Locate every blood parasite and identify its species.
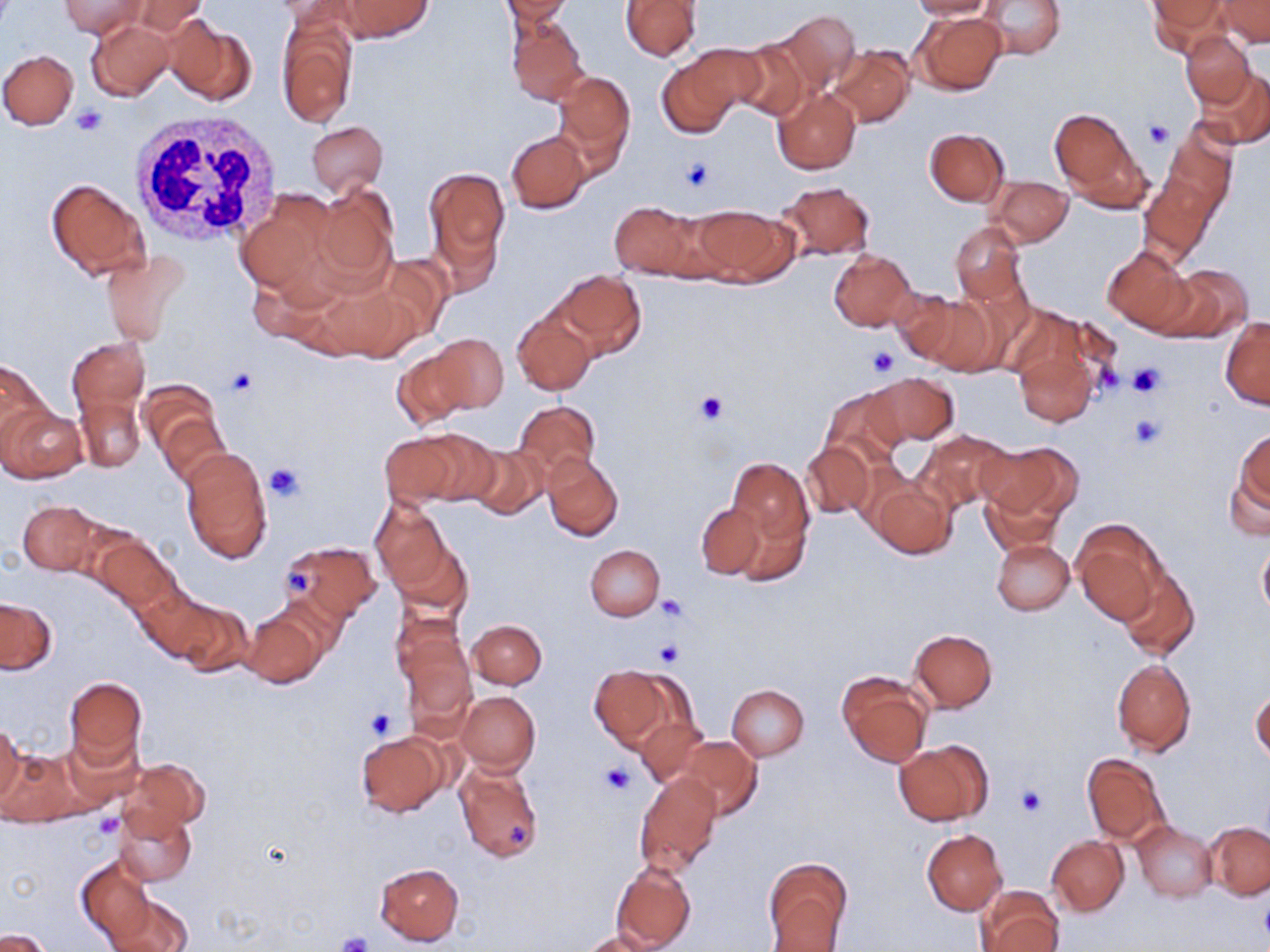

No blood parasites observed.

Approximate bounding boxes as named x1/y1/x2/y2 corners in pixels. Uninfected red blood cell locations: (x1=61, y1=0, x2=143, y2=38), (x1=120, y1=0, x2=213, y2=37), (x1=336, y1=0, x2=432, y2=41), (x1=501, y1=0, x2=573, y2=24), (x1=908, y1=0, x2=1000, y2=20), (x1=980, y1=0, x2=1066, y2=60), (x1=1148, y1=0, x2=1227, y2=53), (x1=621, y1=1, x2=700, y2=60), (x1=1218, y1=1, x2=1270, y2=48), (x1=774, y1=10, x2=860, y2=94), (x1=913, y1=11, x2=1008, y2=95), (x1=277, y1=14, x2=356, y2=129), (x1=506, y1=15, x2=588, y2=106), (x1=167, y1=18, x2=255, y2=108), (x1=86, y1=19, x2=173, y2=102), (x1=1181, y1=32, x2=1255, y2=107), (x1=732, y1=40, x2=810, y2=122), (x1=828, y1=45, x2=914, y2=128), (x1=656, y1=47, x2=753, y2=140), (x1=0, y1=49, x2=78, y2=130), (x1=1195, y1=67, x2=1270, y2=150), (x1=553, y1=70, x2=635, y2=162), (x1=773, y1=86, x2=861, y2=176), (x1=1050, y1=109, x2=1143, y2=205), (x1=306, y1=122, x2=387, y2=198), (x1=924, y1=128, x2=1009, y2=206), (x1=506, y1=130, x2=591, y2=213), (x1=1142, y1=152, x2=1227, y2=259), (x1=423, y1=167, x2=511, y2=275), (x1=986, y1=175, x2=1072, y2=247), (x1=45, y1=177, x2=150, y2=279), (x1=775, y1=181, x2=876, y2=260), (x1=313, y1=183, x2=398, y2=290), (x1=239, y1=188, x2=338, y2=294), (x1=609, y1=201, x2=701, y2=279), (x1=692, y1=204, x2=796, y2=286), (x1=951, y1=221, x2=1028, y2=305), (x1=1102, y1=245, x2=1195, y2=335), (x1=101, y1=249, x2=189, y2=344), (x1=828, y1=249, x2=915, y2=331), (x1=1157, y1=266, x2=1251, y2=341), (x1=551, y1=270, x2=646, y2=358), (x1=893, y1=289, x2=965, y2=363), (x1=912, y1=292, x2=1000, y2=377), (x1=513, y1=310, x2=595, y2=395), (x1=1221, y1=317, x2=1269, y2=409), (x1=1013, y1=333, x2=1104, y2=428), (x1=430, y1=334, x2=509, y2=413), (x1=68, y1=338, x2=149, y2=422), (x1=393, y1=348, x2=474, y2=427), (x1=0, y1=357, x2=51, y2=447), (x1=867, y1=372, x2=959, y2=446), (x1=137, y1=379, x2=224, y2=467), (x1=821, y1=387, x2=906, y2=471), (x1=77, y1=396, x2=144, y2=472), (x1=512, y1=401, x2=601, y2=483), (x1=1, y1=405, x2=87, y2=482), (x1=157, y1=411, x2=229, y2=490), (x1=1234, y1=427, x2=1269, y2=517), (x1=914, y1=431, x2=1015, y2=515), (x1=379, y1=432, x2=468, y2=507), (x1=980, y1=442, x2=1079, y2=521), (x1=465, y1=443, x2=550, y2=520), (x1=802, y1=443, x2=874, y2=518), (x1=180, y1=447, x2=272, y2=564), (x1=542, y1=453, x2=623, y2=542), (x1=1224, y1=454, x2=1270, y2=544), (x1=726, y1=458, x2=813, y2=550), (x1=850, y1=460, x2=920, y2=532), (x1=872, y1=481, x2=956, y2=559), (x1=980, y1=481, x2=1065, y2=558), (x1=370, y1=499, x2=452, y2=592), (x1=17, y1=501, x2=102, y2=575), (x1=695, y1=502, x2=770, y2=581), (x1=732, y1=505, x2=811, y2=587), (x1=1072, y1=520, x2=1163, y2=623), (x1=93, y1=534, x2=179, y2=614), (x1=388, y1=534, x2=472, y2=619), (x1=991, y1=539, x2=1074, y2=615), (x1=283, y1=540, x2=381, y2=623), (x1=1256, y1=542, x2=1270, y2=622), (x1=585, y1=545, x2=664, y2=620), (x1=1115, y1=564, x2=1200, y2=661), (x1=136, y1=588, x2=228, y2=665), (x1=268, y1=592, x2=350, y2=674), (x1=166, y1=597, x2=253, y2=676), (x1=0, y1=598, x2=56, y2=673), (x1=240, y1=608, x2=323, y2=689), (x1=392, y1=615, x2=473, y2=711), (x1=468, y1=620, x2=546, y2=689), (x1=910, y1=629, x2=998, y2=712), (x1=1112, y1=659, x2=1196, y2=756), (x1=589, y1=664, x2=682, y2=750), (x1=836, y1=673, x2=932, y2=768), (x1=65, y1=676, x2=147, y2=770), (x1=726, y1=684, x2=809, y2=760), (x1=1250, y1=687, x2=1269, y2=767), (x1=456, y1=691, x2=541, y2=774), (x1=635, y1=715, x2=705, y2=787), (x1=0, y1=719, x2=24, y2=807), (x1=356, y1=732, x2=446, y2=817), (x1=676, y1=735, x2=762, y2=820), (x1=895, y1=741, x2=991, y2=826), (x1=2, y1=743, x2=86, y2=827), (x1=1083, y1=753, x2=1168, y2=845), (x1=120, y1=759, x2=208, y2=835), (x1=453, y1=759, x2=543, y2=863), (x1=634, y1=772, x2=722, y2=875), (x1=114, y1=809, x2=196, y2=886), (x1=1133, y1=821, x2=1218, y2=901), (x1=1205, y1=821, x2=1270, y2=900), (x1=922, y1=829, x2=1007, y2=914), (x1=1047, y1=836, x2=1129, y2=915), (x1=76, y1=856, x2=156, y2=946), (x1=764, y1=856, x2=853, y2=951), (x1=374, y1=862, x2=464, y2=946), (x1=611, y1=862, x2=696, y2=950), (x1=976, y1=887, x2=1062, y2=951), (x1=107, y1=893, x2=194, y2=952), (x1=1, y1=928, x2=54, y2=951), (x1=581, y1=929, x2=657, y2=952). Platelet locations: (x1=73, y1=105, x2=109, y2=137), (x1=1142, y1=119, x2=1175, y2=148), (x1=677, y1=156, x2=715, y2=194), (x1=868, y1=346, x2=899, y2=376), (x1=1126, y1=361, x2=1166, y2=398), (x1=225, y1=367, x2=257, y2=398), (x1=693, y1=391, x2=729, y2=425), (x1=1129, y1=412, x2=1165, y2=450), (x1=264, y1=462, x2=307, y2=504), (x1=285, y1=564, x2=318, y2=596), (x1=656, y1=595, x2=688, y2=623), (x1=654, y1=640, x2=684, y2=667), (x1=364, y1=707, x2=400, y2=742), (x1=599, y1=761, x2=638, y2=798), (x1=1013, y1=784, x2=1046, y2=818), (x1=93, y1=814, x2=122, y2=838), (x1=506, y1=821, x2=531, y2=853), (x1=334, y1=933, x2=371, y2=952). White blood cell locations: (x1=132, y1=110, x2=282, y2=247). Slide-level diagnosis: no evidence of blood parasites. 1000x magnification. Image is 1270×952 pixels. May-Grünwald-Giemsa-stained preparation. Single field of view. Thin blood film. Optical microscopy.